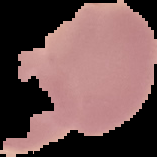

Summary:
  - Image type: cell region segmented out of the field of view; surrounding area masked to black
  - Result: no Plasmodium parasites seen
  - Image size: 157×157 pixels
  - Preparation: thin blood smear